Assess this cell for malaria.
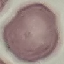
It is uninfected.

Summary:
  - Preparation: thin smear
  - Stain: Giemsa
  - Image type: cell patch, automatically extracted from a larger field of view and resized to 64 × 64 pixels
  - Capture: smartphone camera at the microscope eyepiece